Locate every blood parasite and identify its species.
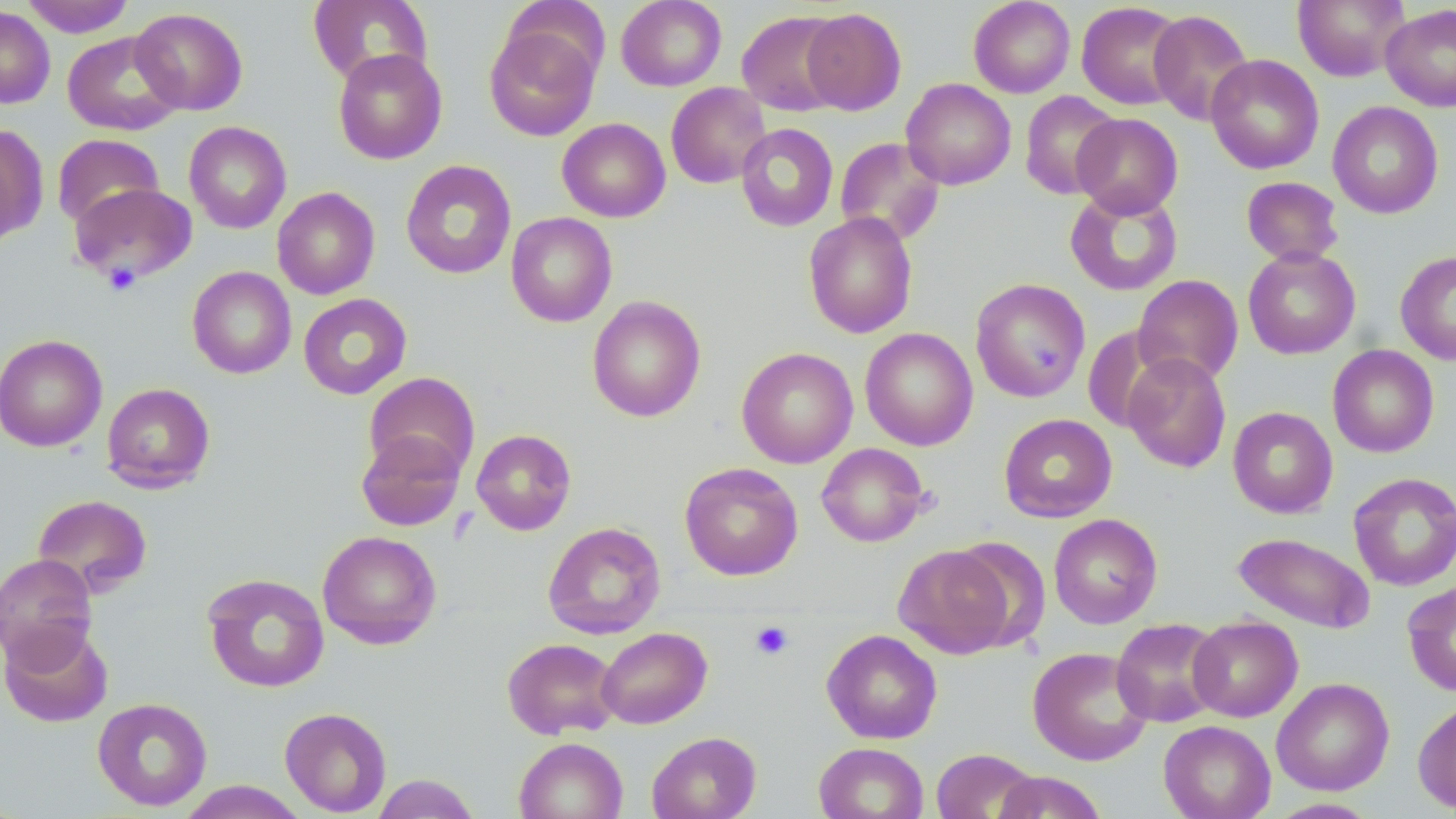
No blood parasites seen.

slide-level diagnosis = negative for blood parasites
field of view = one of a larger specimen
modality = optical microscopy
preparation = thin blood smear
image size = 1456×819 pixels
magnification = 1000x
uninfected red blood cell locations = approximate bounding boxes as (x1, y1, x2, y2) in pixels: (20, 0, 135, 37), (616, 0, 726, 91), (969, 0, 1075, 98), (1293, 0, 1410, 82), (307, 1, 433, 86), (1076, 2, 1187, 110), (1380, 4, 1456, 112), (0, 6, 55, 109), (130, 7, 248, 115), (801, 8, 907, 114), (737, 10, 848, 116), (1148, 10, 1254, 126), (484, 21, 601, 141), (62, 31, 183, 136), (332, 48, 448, 165), (1205, 54, 1324, 174), (901, 79, 1016, 190), (666, 82, 771, 189), (1019, 91, 1122, 200), (1327, 101, 1444, 219), (1071, 113, 1183, 218), (557, 117, 671, 222), (184, 121, 291, 234), (735, 123, 838, 232), (0, 124, 48, 244), (52, 133, 164, 230), (835, 137, 946, 246), (400, 160, 517, 279), (1241, 176, 1344, 266), (69, 182, 198, 285), (272, 187, 380, 299), (1064, 187, 1183, 296), (506, 212, 617, 327), (803, 212, 918, 338), (1243, 246, 1361, 360), (1395, 250, 1456, 365), (187, 266, 296, 379), (1132, 274, 1243, 387), (970, 278, 1091, 402), (298, 293, 412, 399), (587, 295, 706, 423), (1083, 326, 1174, 432), (860, 327, 978, 451), (0, 333, 108, 452), (1327, 344, 1439, 458), (736, 347, 858, 468), (1121, 352, 1231, 474), (364, 372, 480, 481), (101, 382, 216, 493), (1227, 406, 1338, 518), (999, 414, 1117, 523), (471, 429, 577, 535), (356, 430, 466, 531), (816, 442, 929, 547), (679, 462, 803, 581), (1348, 471, 1456, 591), (32, 494, 153, 598), (1048, 513, 1163, 629), (543, 521, 666, 639), (316, 530, 442, 650), (1232, 532, 1376, 633), (893, 544, 1015, 659), (0, 553, 98, 668), (202, 573, 330, 693), (1402, 580, 1456, 697), (1188, 615, 1303, 722), (1111, 618, 1226, 727), (1, 621, 113, 728), (596, 626, 712, 729), (822, 629, 942, 744), (502, 637, 621, 739), (1027, 646, 1152, 766), (1271, 677, 1395, 796), (92, 697, 213, 811), (1413, 698, 1456, 813), (279, 706, 392, 816), (1159, 720, 1275, 819), (647, 731, 761, 819), (514, 737, 628, 819), (814, 742, 928, 818), (931, 748, 1040, 819), (993, 771, 1108, 819), (371, 774, 480, 818), (176, 781, 310, 818), (1266, 797, 1383, 818)
platelet locations = approximate bounding boxes as (x1, y1, x2, y2) in pixels: (104, 262, 141, 295), (750, 621, 794, 660)
stain = May-Grünwald-Giemsa